Describe the morphology of the red blood cells.
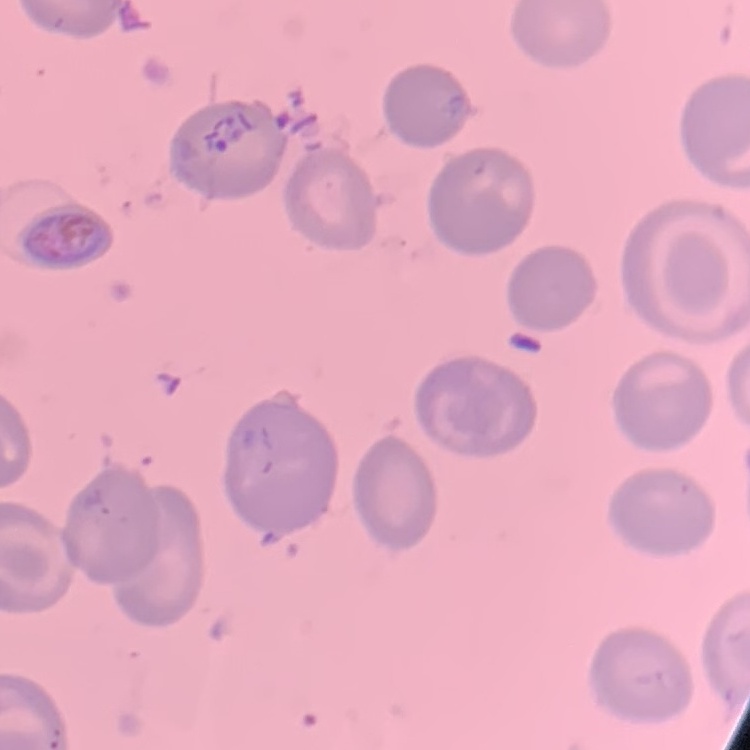
No rouleaux formation.

{
  "stain": "Field's or Giemsa",
  "preparation": "thin peripheral smear",
  "image_type": "one tile cut from a larger photomicrograph"
}